Classify this cell by malaria status.
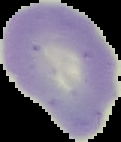
It is uninfected.

preparation = thin blood smear
image size = 121×142 pixels
image type = segmented cell region on a black background